Assess this cell for malaria.
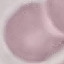
It is uninfected.

Giemsa-stained preparation. Cell patch, automatically extracted from a larger field of view and resized to 64 × 64 pixels. Photographed with a smartphone camera at the microscope eyepiece. Thin smear of blood.